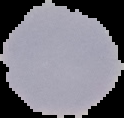

Malaria status: uninfected. Image is 124×118 pixels. The area outside the segmented cell region is set to black. From a thin blood smear.